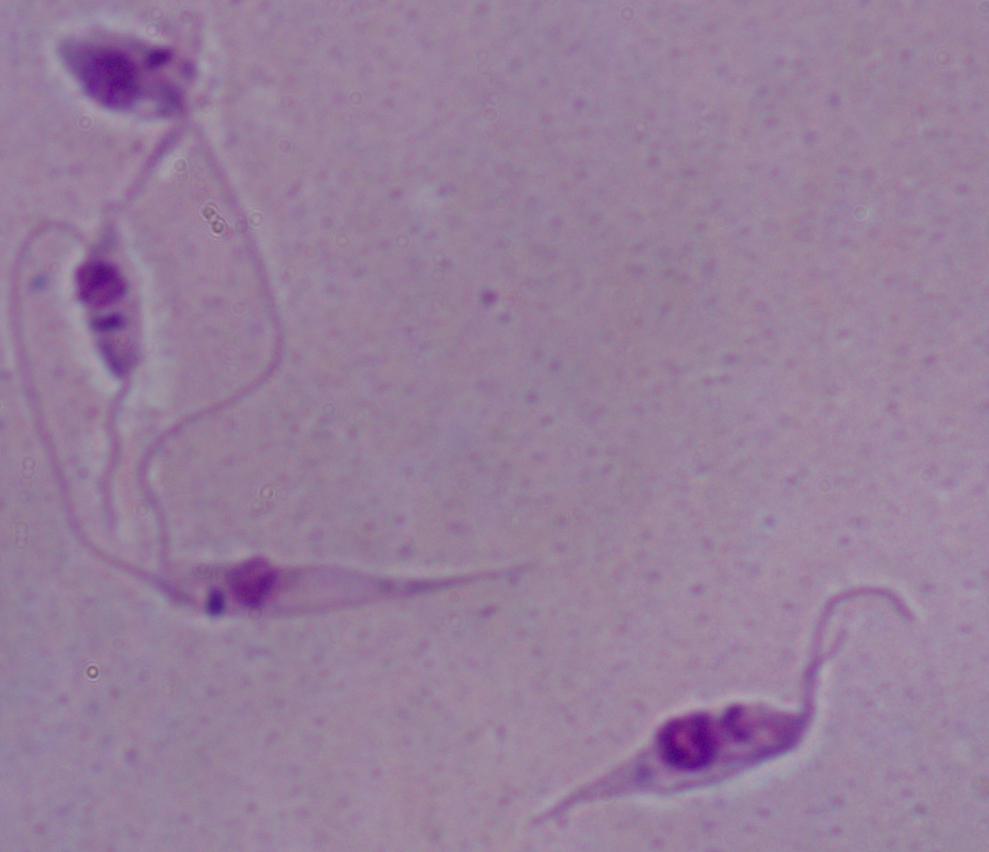
Captured at 1000x magnification. A Leishmania parasite is seen. Photomicrograph.